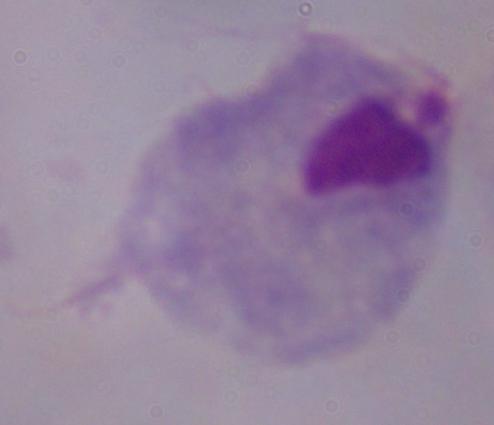
identification = trichomonad
magnification = 1000x
modality = micrograph